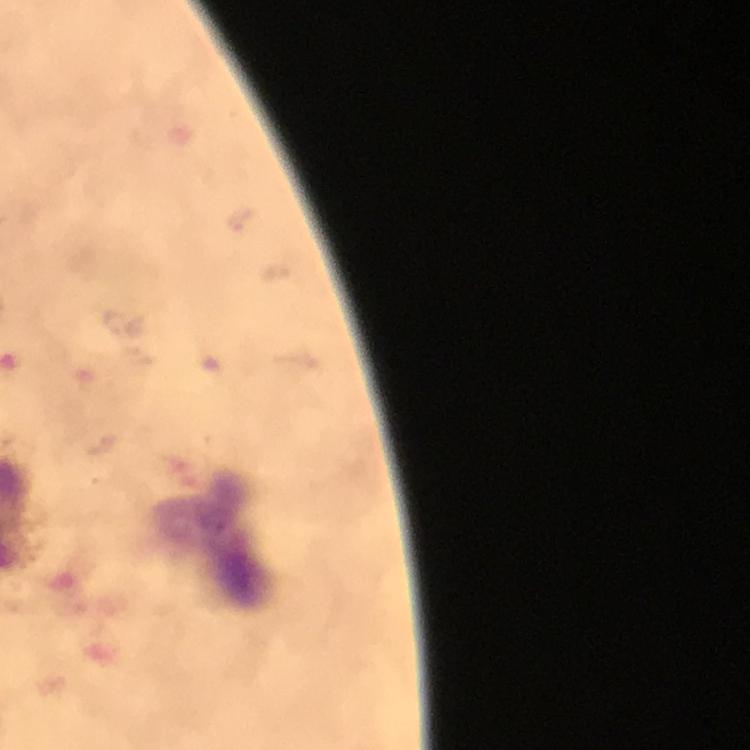

Approximate centers as (x, y) in pixels. Leukocyte locations: (217, 541). From a malaria diagnostic workup. Thick smear. Immersion oil applied. Cropped region of a single field of view. Photographed with a smartphone mounted on the microscope. Giemsa-stained preparation. At 100x magnification. Plasmodium parasites: none seen. Image is 750×750 pixels.